Give the position of every Plasmodium parasite visible.
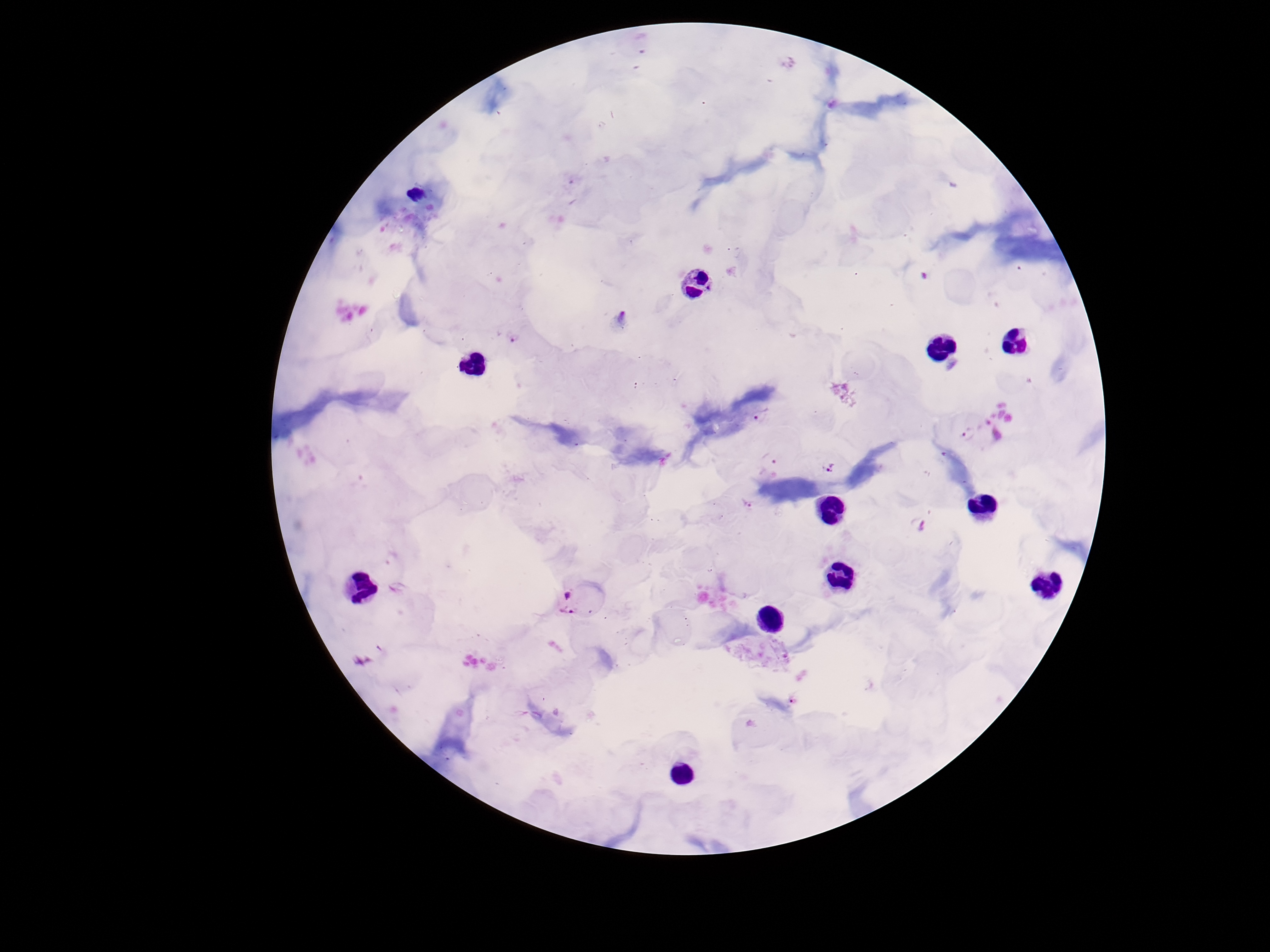

Approximate centers as (x, y) in pixels.
Plasmodium parasites: (831, 101), (621, 316), (514, 337), (764, 414), (969, 434), (769, 460), (833, 469), (748, 503), (920, 524), (567, 601).

magnification: 100x
capture: smartphone camera through the microscope eyepiece
patient_malaria_status: infected
image_size: 1270×952 pixels
stain: Giemsa
preparation: thick peripheral-blood smear
field_of_view: one from this slide